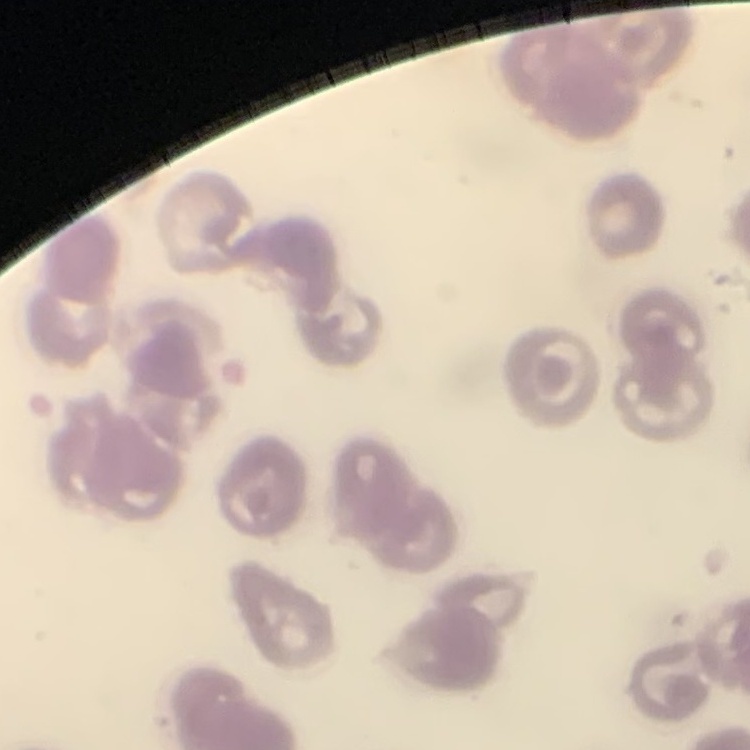
red blood cell morphology = no rouleaux formation
image type = square crop of a larger photomicrograph
stain = Field's or Giemsa
preparation = thin peripheral smear